State which cell type is depicted.
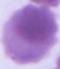

An erythrocyte.

Summary:
  - Magnification: 1000x
  - Modality: photomicrograph